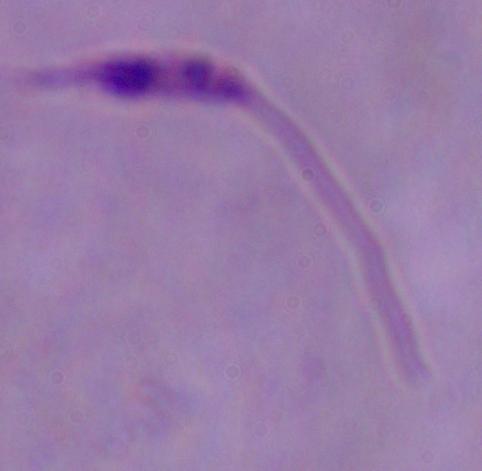
Summary:
  - Magnification: 1000x
  - Modality: micrograph
  - Identification: Leishmania